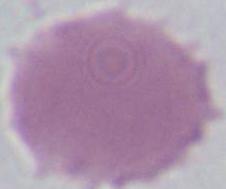
{
  "modality": "photomicrograph",
  "magnification": "1000x",
  "identification": "erythrocyte"
}